Locate and identify every blood parasite.
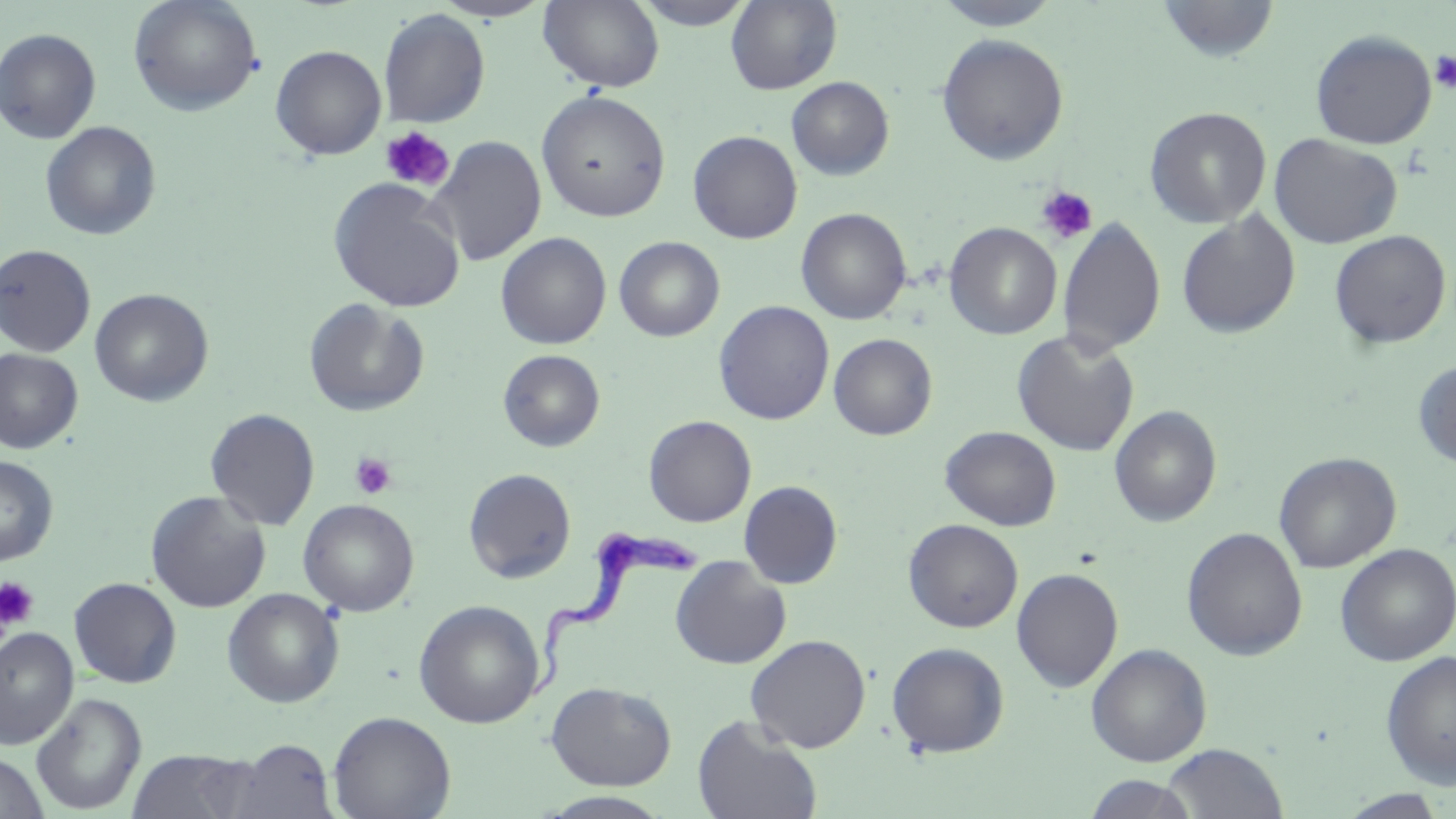
Approximate bounding boxes as (x1, y1, x2, y2) in pixels.
Trypanosoma brucei: (530, 529, 708, 704).
No Plasmodium falciparum, Plasmodium ovale, Plasmodium malariae, Plasmodium vivax, or Babesia divergens observed.

Summary:
  - Platelet locations: (1429, 50, 1456, 93), (380, 126, 455, 192), (1036, 185, 1098, 244), (349, 452, 397, 499), (0, 577, 39, 632)
  - Uninfected red blood cell locations: (432, 0, 554, 22), (539, 0, 665, 93), (631, 0, 757, 30), (726, 0, 842, 95), (930, 0, 1065, 30), (1157, 0, 1280, 63), (128, 1, 262, 116), (379, 9, 490, 128), (0, 28, 101, 144), (1310, 29, 1437, 149), (936, 34, 1069, 165), (270, 45, 387, 160), (786, 76, 894, 180), (536, 90, 671, 222), (1144, 106, 1272, 229), (40, 121, 162, 241), (688, 130, 802, 244), (1269, 133, 1403, 249), (428, 136, 547, 267), (328, 179, 465, 312), (796, 208, 912, 325), (1176, 212, 1300, 339), (1057, 218, 1165, 357), (944, 222, 1062, 339), (1328, 229, 1452, 349), (495, 232, 612, 350), (614, 236, 724, 341), (0, 244, 96, 357), (90, 288, 214, 407), (303, 298, 430, 417), (714, 300, 834, 425), (1011, 330, 1140, 456), (829, 333, 938, 440), (0, 349, 83, 454), (498, 349, 605, 452), (1413, 360, 1456, 469), (1110, 405, 1221, 527), (205, 408, 320, 531), (643, 415, 757, 527), (939, 426, 1062, 531), (1274, 451, 1401, 574), (0, 456, 58, 565), (463, 468, 577, 583), (739, 480, 842, 589), (146, 490, 271, 613), (298, 499, 419, 617), (903, 519, 1023, 633), (1181, 526, 1308, 660), (1335, 543, 1456, 666), (670, 557, 791, 669), (1011, 567, 1123, 692), (68, 577, 182, 688), (222, 588, 344, 707), (414, 599, 545, 728), (0, 626, 78, 750), (745, 634, 871, 753), (886, 641, 1009, 757), (1085, 643, 1212, 766), (1381, 651, 1456, 789), (546, 681, 677, 790), (31, 693, 146, 814), (328, 710, 456, 819), (692, 715, 822, 819), (227, 739, 337, 818), (1162, 744, 1288, 819), (126, 749, 258, 819), (0, 752, 49, 819), (1082, 774, 1198, 818), (1338, 790, 1449, 818), (537, 791, 676, 817)
  - Slide-level diagnosis: Trypanosoma brucei
  - Stain: May-Grünwald-Giemsa
  - Field of view: single
  - Preparation: thin blood smear
  - Image size: 1456×819 pixels
  - Modality: light microscopy
  - Magnification: 1000x